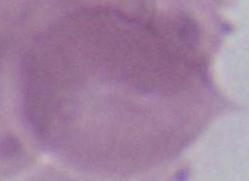

modality: photomicrograph
magnification: 1000x
identification: red blood cell